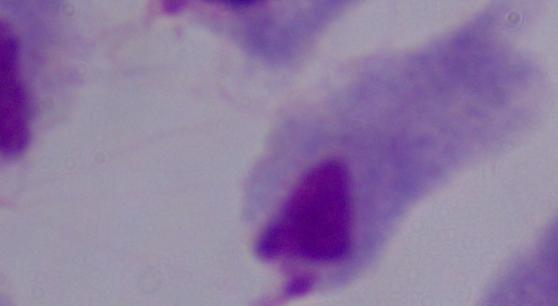
{
  "modality": "micrograph",
  "identification": "trichomonad",
  "magnification": "1000x"
}